Classify this cell by malaria status.
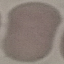

Uninfected.

Cell patch, automatically extracted from a larger field of view and resized to 64 × 64 pixels. Photographed with a smartphone camera at the microscope eyepiece. Thin blood film. Giemsa-stained preparation.